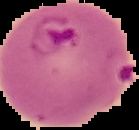
image_size: 139×130 pixels
result: Plasmodium parasites detected
image_type: segmented cell region on a black background
preparation: thin blood film